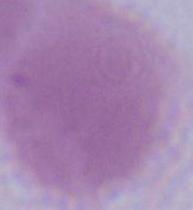

Photomicrograph. 1000x magnification. An erythrocyte is seen.